Comment on the morphology of the red blood cells.
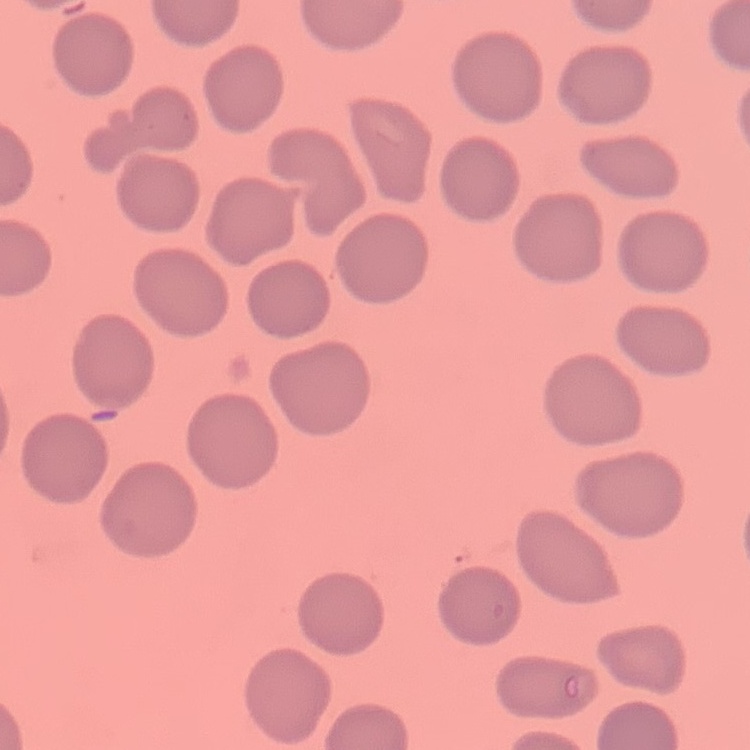
No rouleaux formation.

Summary:
  - Image type: square crop of a larger photomicrograph
  - Preparation: thin blood smear
  - Stain: Field's or Giemsa